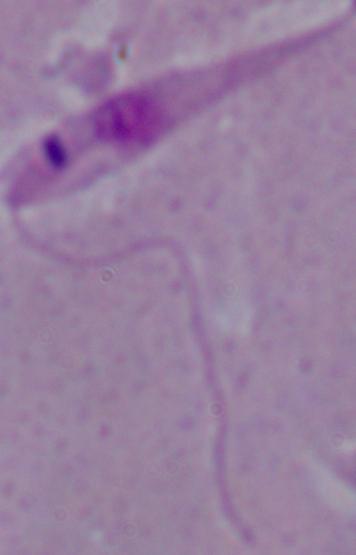
A Leishmania parasite is seen. 1000x magnification. Photomicrograph.